Name the parasite shown.
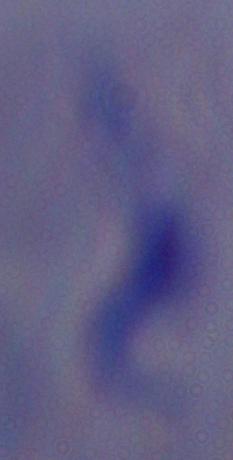
This is a trypanosome.

magnification = 1000x
modality = micrograph